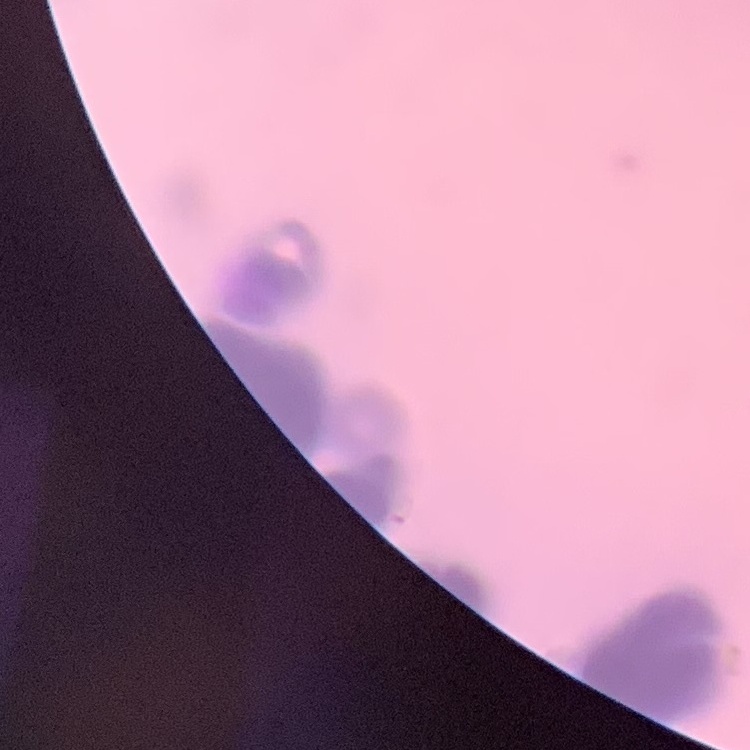
The erythrocytes show rouleaux formation. Thin peripheral smear. Square crop of a larger photomicrograph. Field's or Giemsa stain.